Point out each leukocyte.
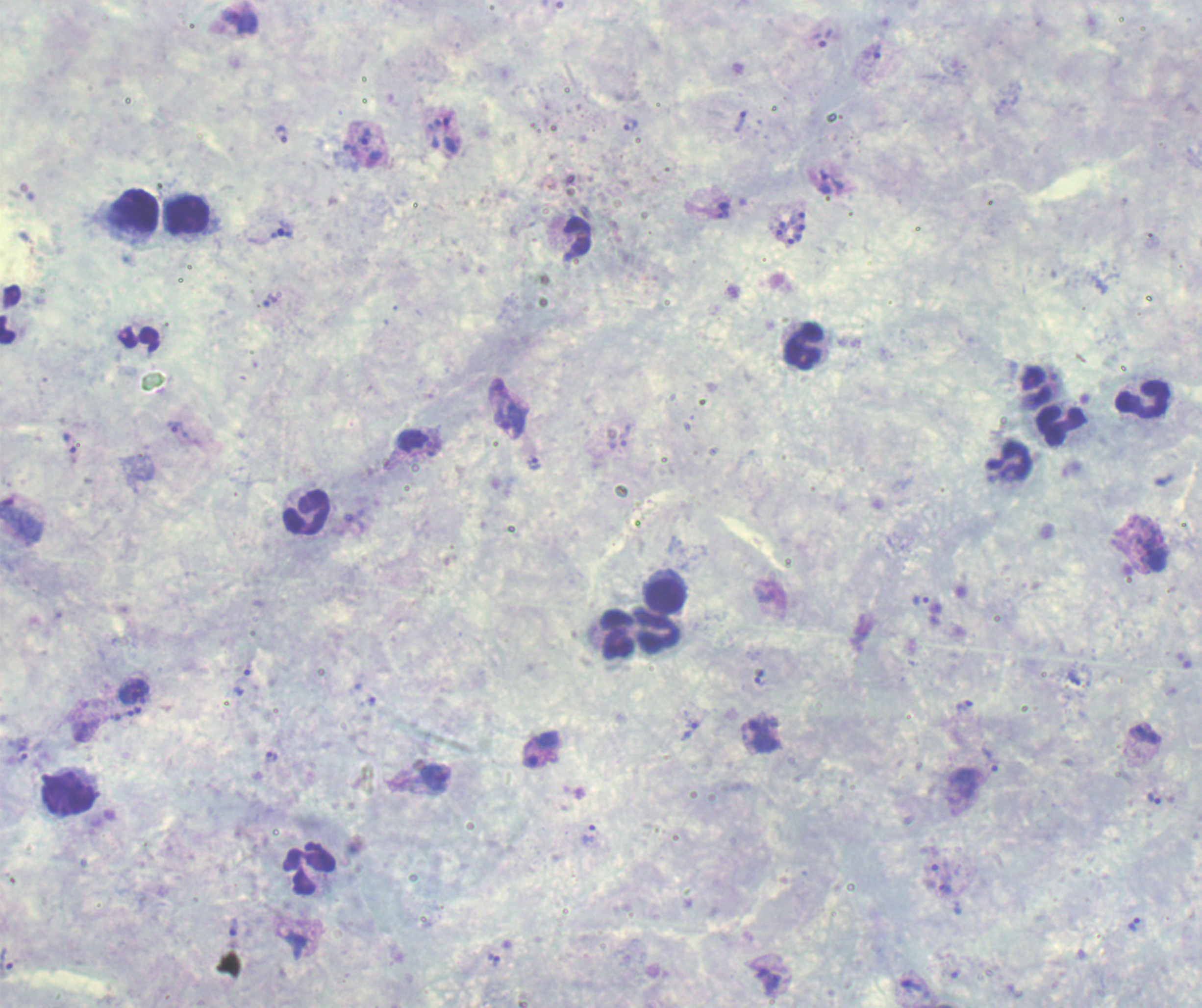

Approximate centers as [x, y] in pixels.
Leukocytes: [134, 211], [185, 215], [577, 239], [10, 315], [139, 339], [803, 346], [1035, 387], [1143, 397], [1060, 425], [1009, 459], [306, 512], [665, 595], [658, 631], [616, 633], [68, 794], [309, 868].

Approximate centers as [x, y] in pixels. Trophozoite locations: [240, 21], [822, 36], [872, 59], [740, 121], [630, 125], [442, 132], [281, 134], [367, 145], [830, 181], [722, 210], [282, 231], [269, 300], [500, 390], [510, 422], [183, 434], [616, 436], [414, 441], [71, 446], [535, 462], [354, 521], [1155, 556], [922, 599], [242, 676], [760, 676], [1075, 679], [133, 692], [372, 701], [964, 706], [138, 709], [122, 714], [85, 729], [690, 729], [1143, 733], [761, 734], [541, 749], [22, 753], [270, 758], [989, 759], [435, 778], [1153, 799], [590, 837], [939, 875], [958, 908], [1136, 924], [233, 927], [296, 945], [495, 960], [7, 963], [956, 973], [769, 976], [914, 988]. Schizont locations: [788, 227]. Life-cycle stages observed: trophozoite, schizont. Thick blood smear. Previously used in an actual diagnosis. Background quality: unsatisfactory. Image is 1202×1008 pixels. 100x magnification. Romanowsky stain. Result: malaria parasites identified. One field from this slide.